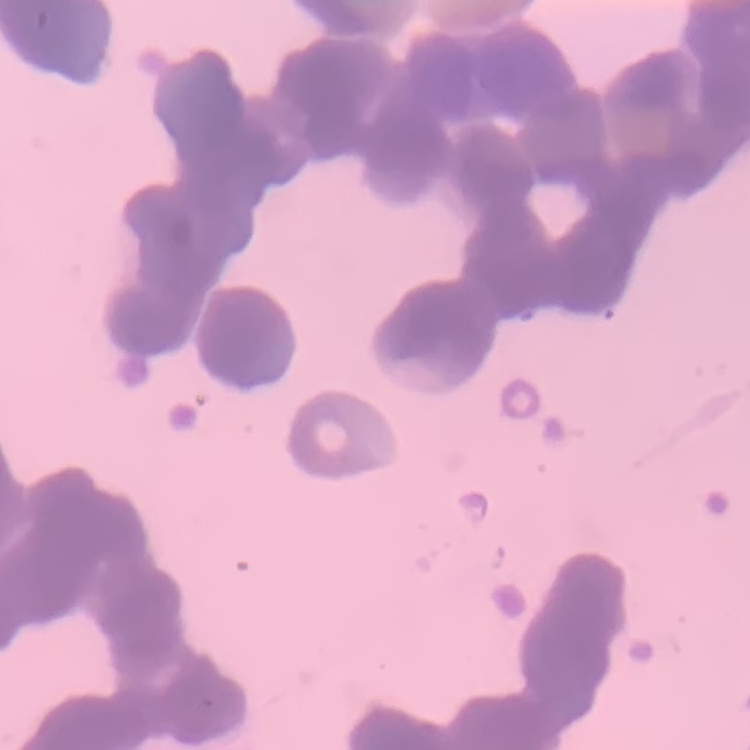 The red blood cells show rouleaux formation. Square crop of a larger photomicrograph. Thin blood film. Field's or Giemsa stain.